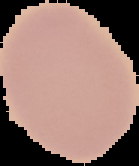
Summary:
  - Result: negative for Plasmodium parasites
  - Preparation: thin blood film
  - Image size: 139×166 pixels
  - Image type: cell region segmented out of the field of view; surrounding area masked to black